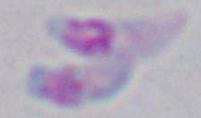

Summary:
  - Modality: photomicrograph
  - Magnification: 1000x
  - Identification: Toxoplasma gondii